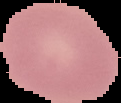
Summary:
  - Image size: 121×103 pixels
  - Image type: segmented cell region on a black background
  - Result: no malaria parasites detected
  - Preparation: thin blood film